Identify the blood parasite species.
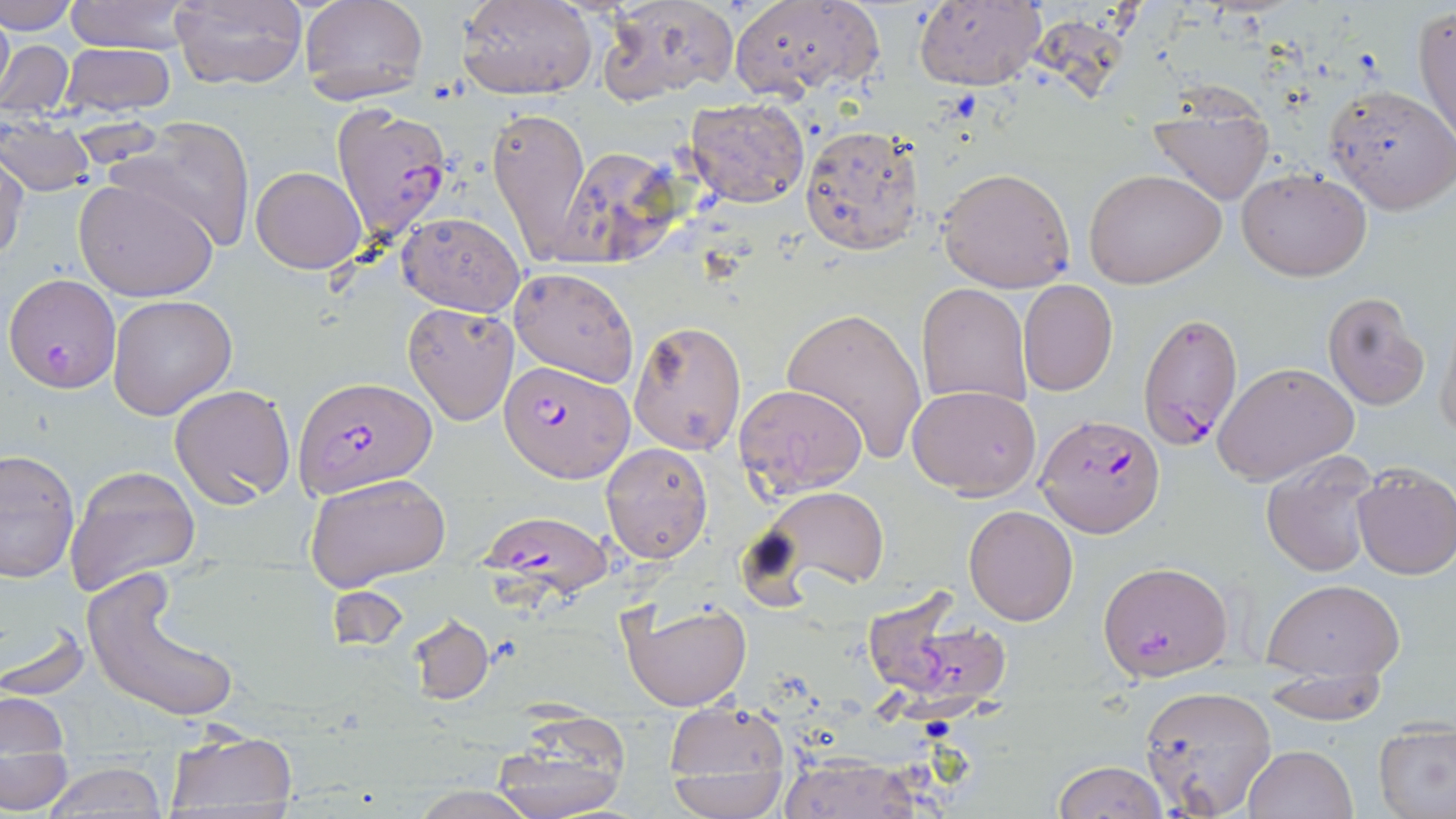
Plasmodium falciparum.

Summary:
  - Coordinate format: approximate bounding boxes as (x1, y1, x2, y2) in pixels
  - Plasmodium falciparum-infected red blood cell locations: (331, 104, 453, 244), (5, 273, 121, 390), (1137, 310, 1244, 452), (499, 361, 632, 482), (293, 376, 434, 501), (1035, 413, 1166, 537), (477, 507, 613, 604), (1099, 559, 1233, 681), (858, 587, 1012, 716)
  - Uninfected red blood cell locations: (1, 0, 80, 33), (64, 0, 195, 54), (299, 0, 429, 103), (457, 0, 598, 102), (596, 0, 739, 105), (730, 0, 884, 101), (169, 1, 308, 89), (912, 1, 1046, 93), (1413, 4, 1456, 142), (1, 6, 14, 110), (2, 38, 75, 121), (61, 42, 175, 116), (1324, 84, 1456, 212), (1145, 88, 1278, 205), (682, 98, 811, 208), (485, 107, 592, 260), (0, 115, 97, 197), (113, 120, 258, 251), (799, 124, 924, 255), (548, 149, 677, 266), (0, 150, 28, 267), (250, 166, 366, 273), (936, 167, 1077, 292), (1238, 167, 1371, 279), (1083, 168, 1227, 289), (73, 176, 223, 303), (396, 211, 526, 316), (507, 265, 641, 387), (1018, 280, 1118, 396), (917, 283, 1033, 410), (1321, 291, 1431, 410), (107, 296, 237, 419), (403, 302, 520, 425), (781, 305, 927, 464), (1434, 313, 1456, 446), (629, 320, 747, 456), (1212, 361, 1359, 484), (733, 382, 865, 500), (169, 383, 295, 507), (906, 384, 1042, 498), (601, 442, 713, 564), (0, 447, 80, 582), (1261, 456, 1381, 577), (65, 465, 198, 595), (1351, 465, 1456, 580), (302, 473, 451, 591), (751, 485, 889, 597), (963, 504, 1078, 625), (84, 571, 243, 724), (1264, 580, 1405, 684), (617, 598, 750, 712), (1, 613, 90, 700), (407, 614, 494, 703), (1261, 658, 1388, 726), (1136, 683, 1278, 817), (2, 692, 70, 755), (661, 702, 793, 809), (490, 720, 632, 819), (1374, 723, 1456, 819), (162, 728, 298, 813), (1242, 745, 1357, 819), (2, 751, 74, 814), (775, 755, 924, 818), (1052, 760, 1168, 818), (40, 762, 169, 818), (666, 768, 787, 817), (406, 786, 545, 819)
  - Modality: optical microscopy
  - Magnification: 1000x
  - Stain: May-Grünwald-Giemsa
  - Image size: 1456×819 pixels
  - Field of view: single
  - Preparation: thin blood smear